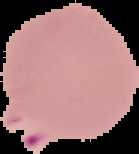

Summary:
  - Image size: 139×154 pixels
  - Malaria status: parasitized
  - Preparation: thin blood film
  - Image type: segmented cell region with the area outside set to black